Locate every malaria parasite.
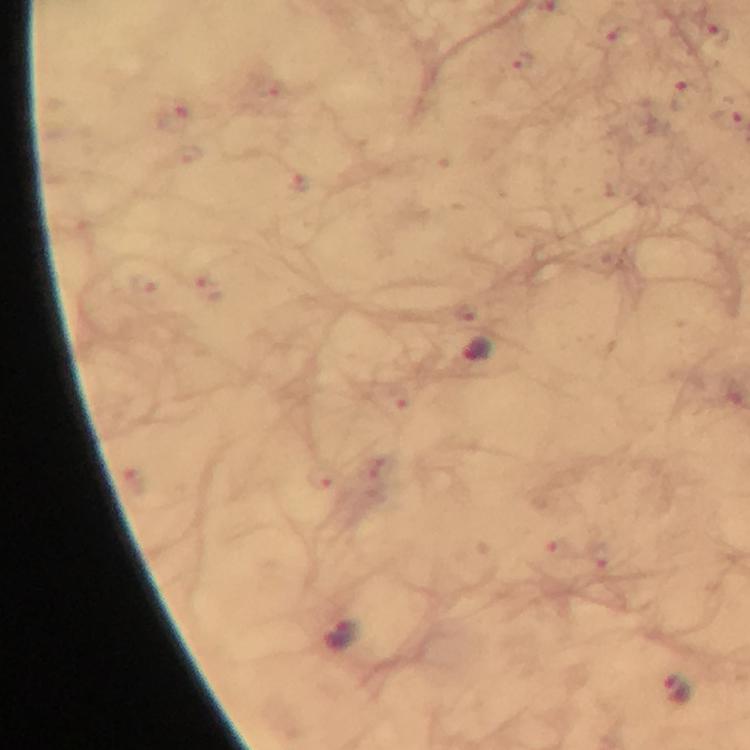
Approximate centers as (x, y) in pixels.
Malaria parasites: (477, 348), (343, 633), (678, 690).

From a diagnostic examination for malaria. Thick blood smear. Image is 750×750 pixels. Giemsa-stained preparation. 100x magnification. Cropped region of a single field of view. Immersion oil was used. Smartphone photograph taken through a microscope.